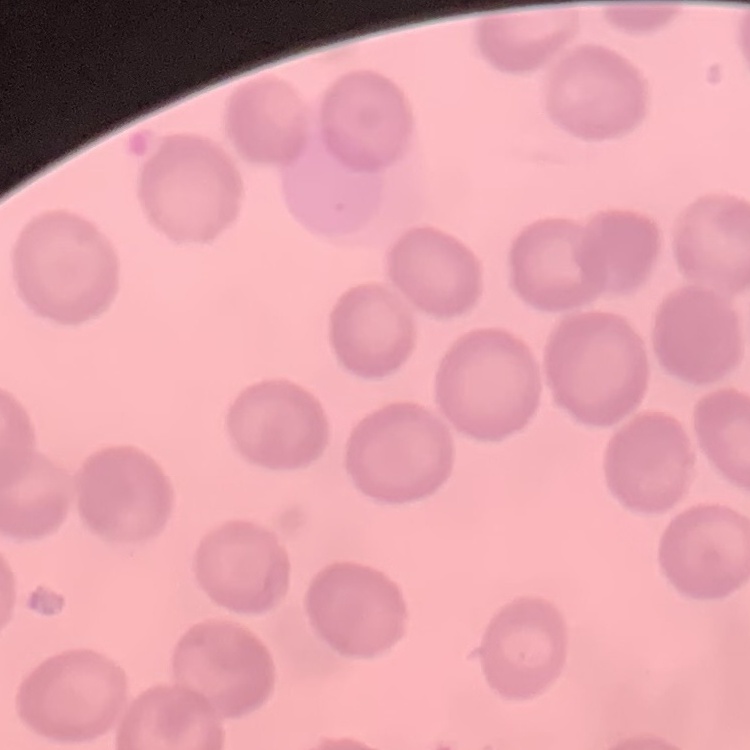

erythrocyte morphology = no rouleaux formation
image type = one tile cut from a larger photomicrograph
stain = Field's or Giemsa
preparation = thin blood smear